Assess this cell for malaria.
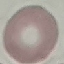

Uninfected.

Giemsa-stained preparation. Thin blood smear. Acquired by smartphone through the microscope eyepiece. Automatically extracted cell patch, resized to 64 × 64 pixels.